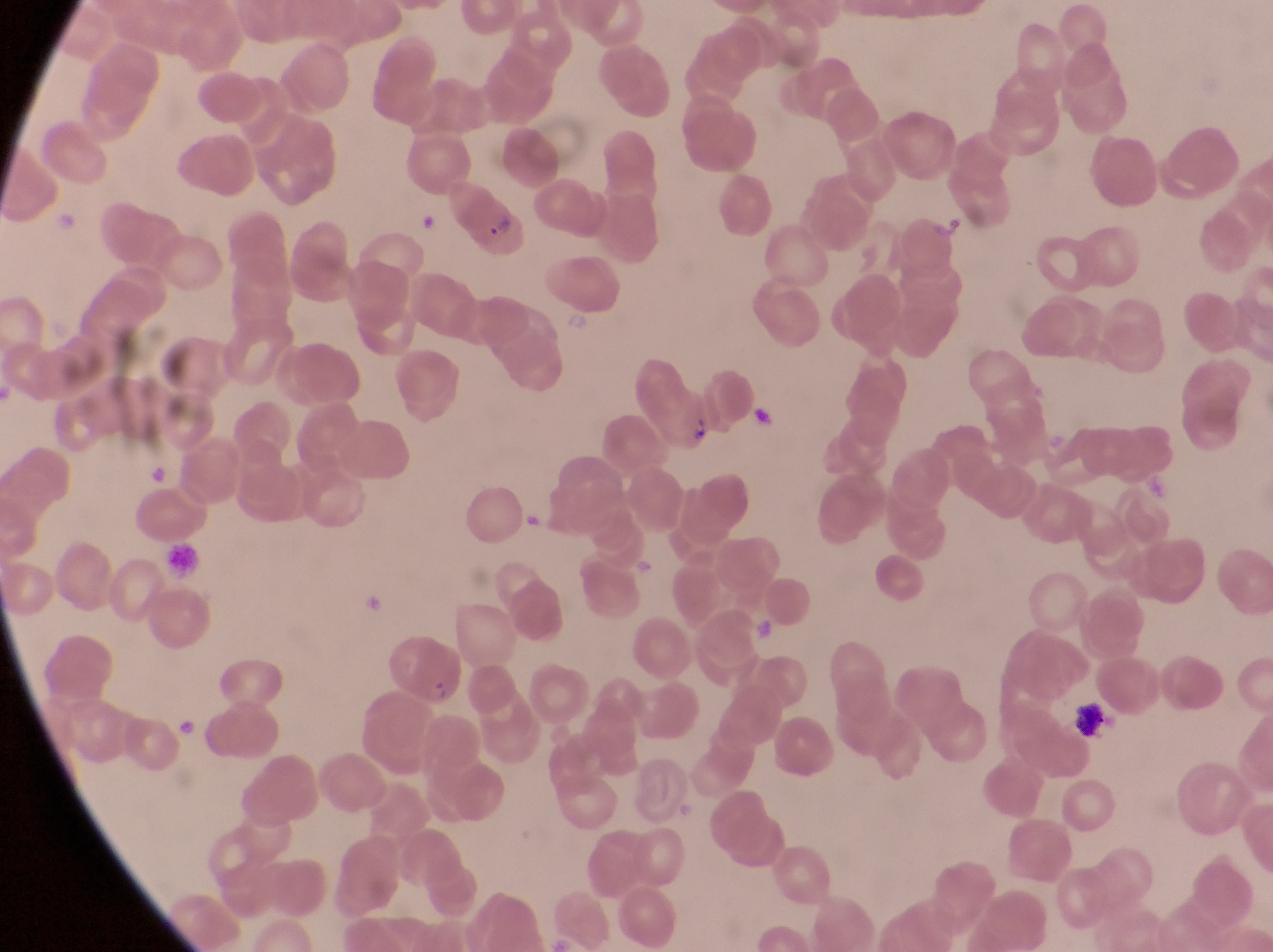
parasitised red blood cell locations = approximate bounding boxes as [left, top, right, bottom] in pixels: [451, 192, 529, 264], [649, 387, 714, 454], [391, 642, 463, 710]
preparation = thin blood film
image size = 1273×952 pixels
capture = smartphone photograph through the eyepiece of an Olympus CX-23 microscope
magnification = 1000x
field of view = single
leukocyte locations = approximate bounding boxes as [left, top, right, bottom] in pixels: [164, 543, 205, 588]
artifact (platelet-like body, stain precipitate, or debris) locations = approximate bounding boxes as [left, top, right, bottom] in pixels: [750, 403, 779, 432], [1066, 692, 1113, 745]
country = Uganda